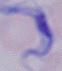

Summary:
  - Magnification: 1000x
  - Modality: photomicrograph
  - Identification: trypanosome